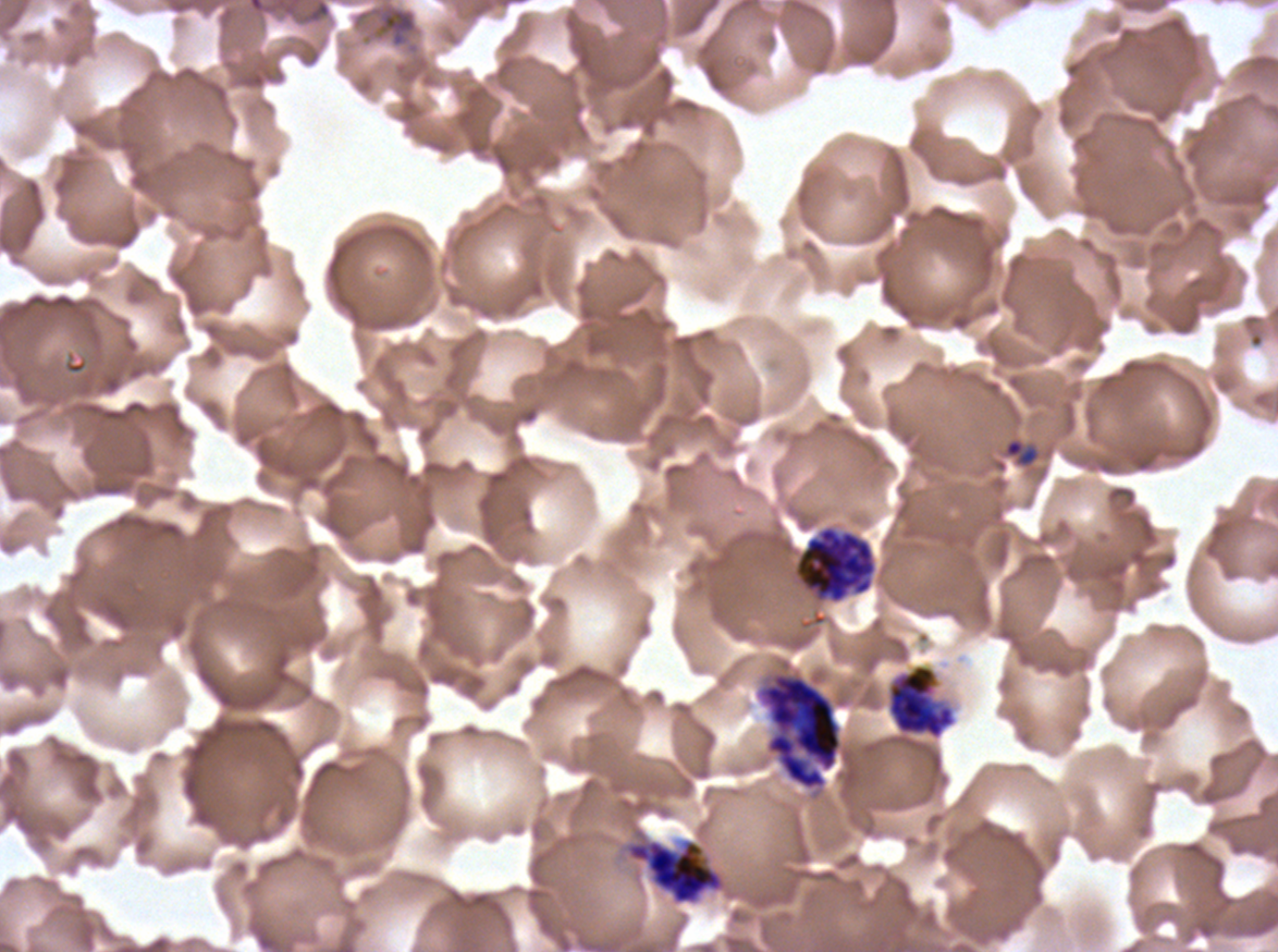

specimen: P. falciparum cultured ex vivo for 24 to 48 hours, from a patient in The Gambia
late_schizont_locations: 'approximate bounding boxes as (x1, y1, x2, y2) in pixels: (754, 670, 843, 791)'
late_ring_early_trophozoite_locations: 'approximate bounding boxes as (x1, y1, x2, y2) in pixels: (1003, 437, 1039, 468)'
preparation: thin blood film
early_schizont_locations: 'approximate bounding boxes as (x1, y1, x2, y2) in pixels: (887, 664, 955, 739), (625, 838, 725, 905)'
segmenter_locations: 'approximate bounding boxes as (x1, y1, x2, y2) in pixels: (793, 525, 877, 604)'
life_cycle_stages_observed: late-ring/early-trophozoite, early schizont, late schizont, segmenter
stain: Giemsa
field_of_view: one sub-image of a larger composite
image_size: 1278×952 pixels
debris_locations: 'approximate bounding boxes as (x1, y1, x2, y2) in pixels: (246, 0, 333, 26), (373, 3, 418, 48)'